Give the extent of all uninfected red blood cells.
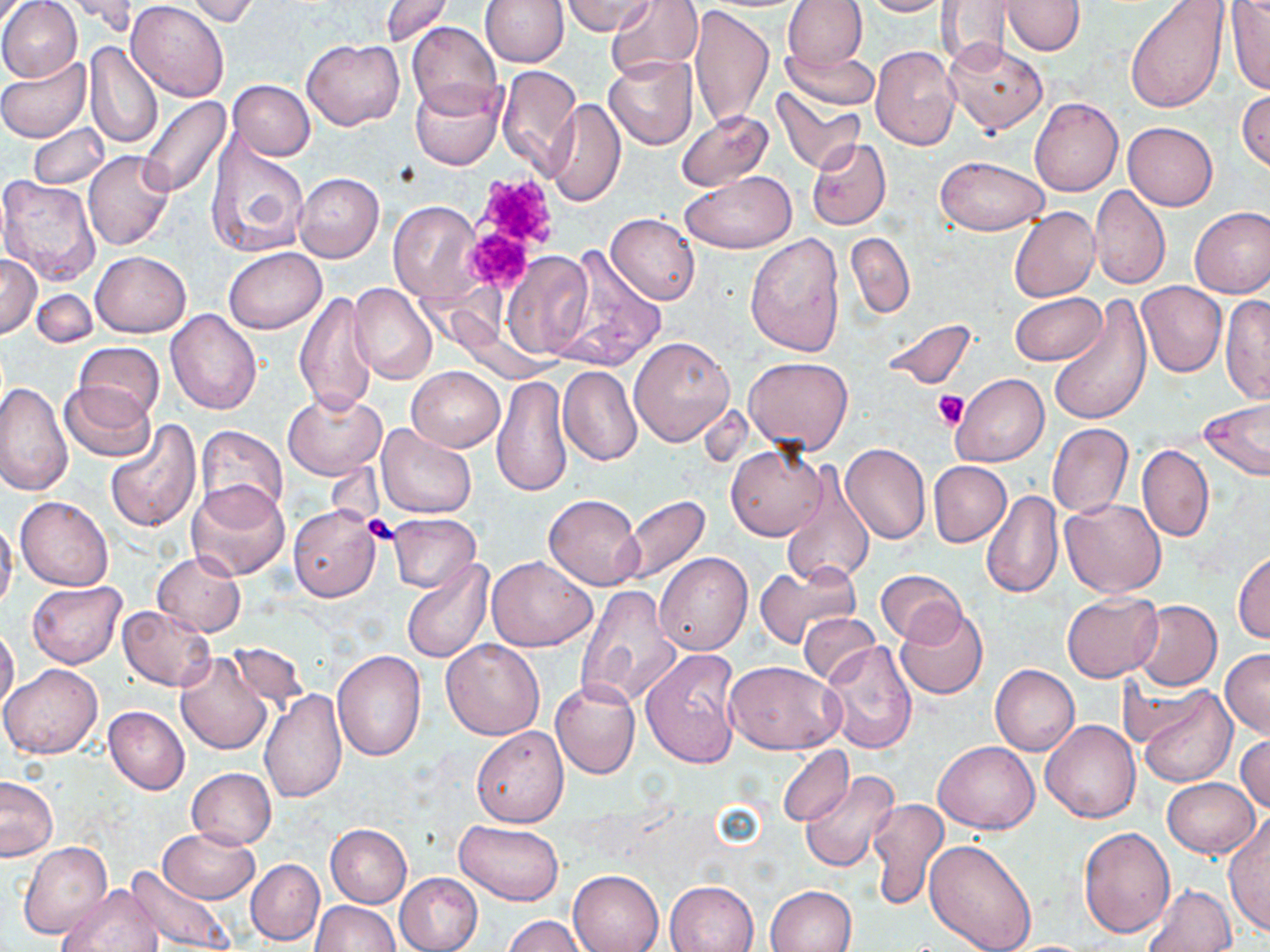

Approximate bounding boxes as [x1, y1, x2, y2] in pixels.
Uninfected red blood cells: [0, 0, 82, 83], [62, 0, 140, 35], [381, 0, 454, 47], [480, 0, 569, 67], [561, 0, 654, 35], [606, 0, 703, 84], [783, 0, 867, 72], [861, 0, 955, 16], [937, 0, 1013, 69], [1126, 0, 1229, 113], [125, 1, 231, 101], [182, 1, 259, 25], [1002, 1, 1086, 56], [689, 3, 774, 132], [1226, 3, 1270, 95], [406, 21, 503, 118], [943, 38, 1047, 135], [303, 39, 403, 130], [84, 43, 162, 149], [782, 46, 879, 111], [870, 46, 961, 152], [604, 56, 699, 149], [0, 58, 91, 142], [495, 64, 582, 174], [228, 80, 316, 160], [410, 80, 506, 170], [772, 87, 864, 175], [1237, 90, 1270, 173], [137, 96, 232, 199], [1030, 98, 1123, 196], [546, 100, 626, 208], [675, 110, 773, 192], [28, 122, 109, 189], [1122, 122, 1218, 210], [205, 133, 309, 258], [807, 138, 891, 231], [84, 151, 175, 250], [936, 156, 1050, 235], [680, 171, 797, 254], [294, 172, 384, 263], [0, 175, 103, 285], [1090, 185, 1170, 290], [389, 201, 482, 302], [1010, 206, 1100, 303], [1190, 207, 1270, 298], [607, 213, 700, 305], [747, 231, 845, 356], [845, 232, 915, 319], [224, 247, 327, 334], [553, 248, 663, 370], [90, 250, 190, 337], [500, 251, 593, 358], [0, 255, 41, 338], [1137, 282, 1226, 377], [349, 284, 437, 386], [31, 289, 98, 347], [295, 289, 377, 416], [1010, 292, 1107, 365], [1219, 295, 1270, 406], [1049, 297, 1152, 428], [166, 309, 262, 414], [881, 318, 978, 389], [629, 335, 735, 447], [74, 342, 165, 423], [743, 357, 853, 456], [406, 366, 505, 451], [558, 366, 642, 467], [951, 373, 1049, 467], [492, 374, 573, 497], [59, 380, 156, 462], [0, 382, 73, 498], [283, 391, 387, 481], [1199, 403, 1270, 482], [102, 419, 202, 534], [375, 423, 479, 519], [1048, 424, 1133, 518], [195, 425, 288, 520], [840, 443, 931, 545], [1138, 445, 1213, 541], [727, 446, 826, 540], [1103, 449, 1203, 576], [929, 461, 1012, 548], [779, 466, 876, 588], [186, 480, 291, 583], [981, 491, 1063, 599], [16, 494, 114, 591], [545, 494, 643, 591], [616, 495, 711, 587], [1058, 498, 1168, 598], [289, 504, 382, 601], [388, 514, 480, 592], [0, 518, 18, 614], [151, 550, 246, 635], [1234, 550, 1270, 644], [655, 552, 752, 656], [487, 555, 597, 652], [400, 558, 495, 664], [753, 562, 861, 648], [876, 569, 968, 646], [28, 581, 125, 669], [574, 585, 681, 708], [1061, 592, 1161, 682], [1132, 600, 1222, 691], [118, 605, 216, 690], [895, 608, 988, 700], [800, 612, 879, 687], [0, 624, 19, 714], [441, 639, 546, 740], [821, 640, 917, 754], [227, 642, 309, 713], [331, 649, 425, 761], [641, 649, 742, 768], [1220, 649, 1270, 739], [174, 652, 274, 755], [725, 661, 844, 755], [2, 663, 104, 759], [990, 664, 1080, 755], [550, 680, 640, 781], [1119, 680, 1210, 749], [1135, 685, 1237, 787], [259, 690, 347, 804], [104, 706, 189, 795], [1041, 719, 1140, 823], [471, 725, 568, 827], [1235, 732, 1270, 813], [933, 741, 1040, 834], [777, 745, 853, 826], [186, 767, 276, 848], [800, 770, 902, 874], [0, 775, 58, 861], [1162, 778, 1260, 857], [866, 797, 950, 910], [1223, 814, 1270, 936], [455, 820, 565, 904], [326, 824, 412, 908], [1079, 826, 1174, 938], [158, 828, 261, 903], [923, 839, 1037, 952], [19, 843, 112, 938], [246, 859, 324, 945], [125, 865, 234, 951], [568, 870, 664, 952], [394, 872, 482, 952], [665, 881, 757, 952], [55, 882, 162, 952], [1142, 884, 1238, 952], [766, 885, 858, 951], [312, 900, 399, 951], [504, 916, 586, 952].

Platelet locations: [467, 176, 561, 275], [462, 228, 532, 292], [933, 390, 968, 428], [362, 516, 401, 545]. Slide-level diagnosis: no evidence of blood parasites. One field of a larger specimen. Thin blood smear. Image is 1270×952 pixels. Optical microscopy. May-Grünwald-Giemsa-stained preparation. Captured at 1000x magnification.